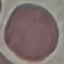
Malaria status: uninfected. Thin blood smear. Giemsa-stained preparation. Cell patch, automatically extracted from a larger field of view and resized to 64 × 64 pixels. Photographed with a smartphone camera at the microscope eyepiece.